State which cell type is depicted.
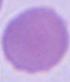
This is an erythrocyte.

Captured at 1000x magnification. Micrograph.